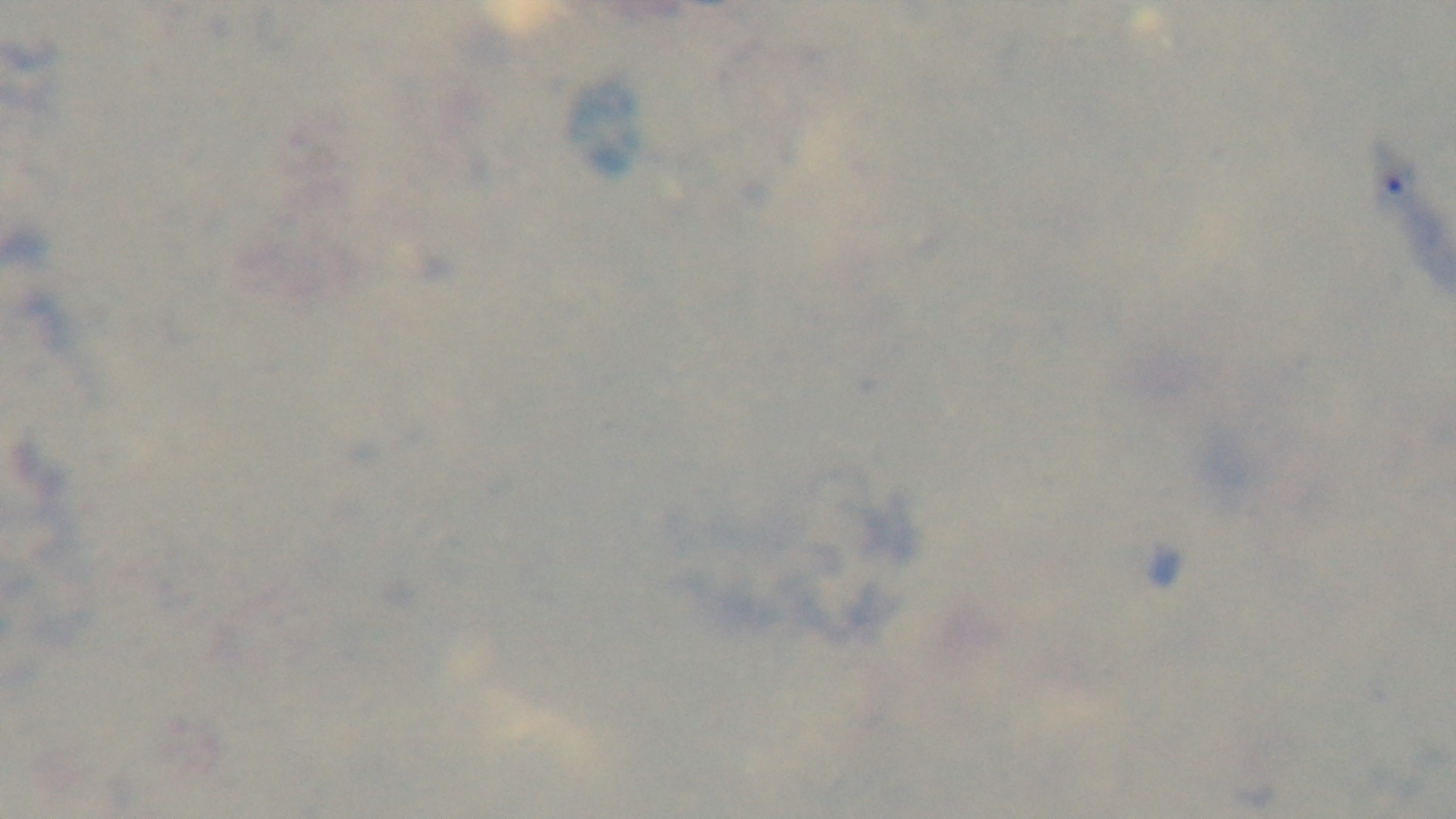

malaria status = uninfected
capture = mounted 4K digital camera
preparation = thick smear
modality = light microscopy
objective = 100x oil immersion
stain = Giemsa
field of view = one from the slide